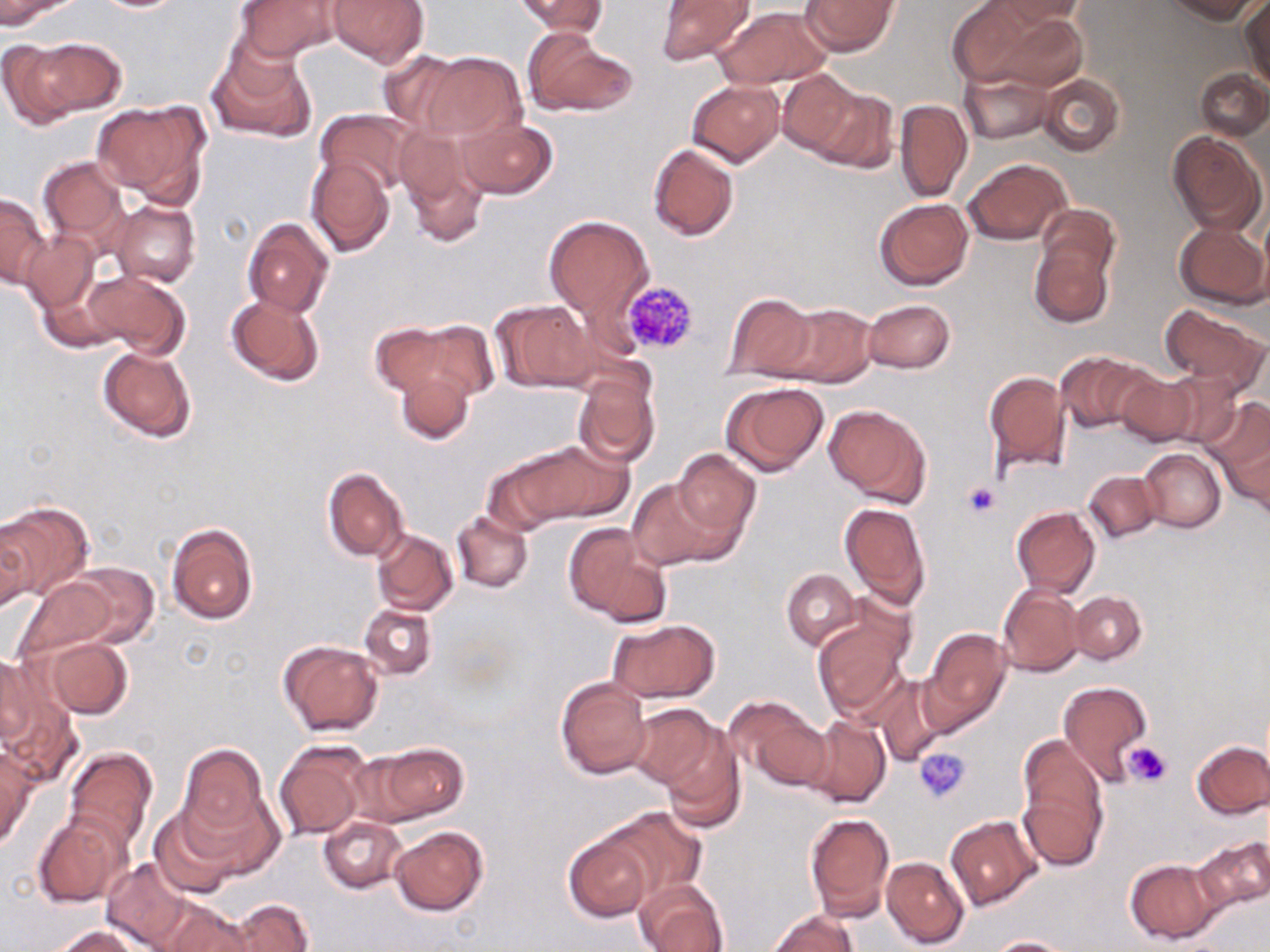
Approximate bounding boxes as named x1/y1/x2/y2 corners in pixels. Uninfected red blood cell locations: (x1=0, y1=0, x2=77, y2=30), (x1=88, y1=0, x2=191, y2=12), (x1=326, y1=0, x2=429, y2=68), (x1=515, y1=0, x2=608, y2=36), (x1=655, y1=0, x2=754, y2=66), (x1=801, y1=0, x2=899, y2=56), (x1=947, y1=0, x2=1043, y2=88), (x1=996, y1=0, x2=1089, y2=26), (x1=1161, y1=0, x2=1263, y2=23), (x1=236, y1=1, x2=342, y2=61), (x1=1240, y1=1, x2=1269, y2=85), (x1=715, y1=6, x2=829, y2=89), (x1=986, y1=10, x2=1090, y2=92), (x1=524, y1=29, x2=637, y2=118), (x1=16, y1=36, x2=124, y2=121), (x1=207, y1=42, x2=315, y2=144), (x1=377, y1=49, x2=468, y2=133), (x1=418, y1=52, x2=526, y2=142), (x1=959, y1=67, x2=1054, y2=144), (x1=1196, y1=69, x2=1269, y2=140), (x1=776, y1=70, x2=862, y2=156), (x1=1038, y1=74, x2=1124, y2=156), (x1=687, y1=79, x2=785, y2=166), (x1=801, y1=82, x2=895, y2=170), (x1=894, y1=99, x2=972, y2=204), (x1=92, y1=101, x2=211, y2=204), (x1=315, y1=109, x2=416, y2=198), (x1=457, y1=116, x2=560, y2=197), (x1=397, y1=125, x2=493, y2=245), (x1=1168, y1=132, x2=1265, y2=235), (x1=647, y1=143, x2=741, y2=241), (x1=36, y1=156, x2=130, y2=251), (x1=307, y1=156, x2=395, y2=257), (x1=963, y1=157, x2=1071, y2=245), (x1=1, y1=193, x2=49, y2=288), (x1=873, y1=198, x2=974, y2=290), (x1=112, y1=200, x2=200, y2=288), (x1=543, y1=215, x2=653, y2=323), (x1=242, y1=217, x2=334, y2=317), (x1=1174, y1=222, x2=1268, y2=310), (x1=23, y1=232, x2=99, y2=312), (x1=1028, y1=232, x2=1117, y2=330), (x1=84, y1=270, x2=189, y2=357), (x1=721, y1=292, x2=819, y2=380), (x1=226, y1=293, x2=325, y2=387), (x1=863, y1=298, x2=954, y2=374), (x1=493, y1=301, x2=600, y2=393), (x1=1159, y1=302, x2=1268, y2=390), (x1=772, y1=304, x2=877, y2=387), (x1=413, y1=319, x2=499, y2=403), (x1=370, y1=324, x2=458, y2=399), (x1=97, y1=345, x2=197, y2=442), (x1=1055, y1=351, x2=1154, y2=434), (x1=391, y1=364, x2=475, y2=446), (x1=983, y1=369, x2=1071, y2=474), (x1=1113, y1=369, x2=1199, y2=447), (x1=572, y1=370, x2=659, y2=468), (x1=1157, y1=372, x2=1245, y2=450), (x1=722, y1=381, x2=829, y2=476), (x1=1203, y1=396, x2=1269, y2=496), (x1=825, y1=404, x2=932, y2=508), (x1=1224, y1=428, x2=1270, y2=516), (x1=499, y1=441, x2=627, y2=527), (x1=1138, y1=447, x2=1225, y2=532), (x1=672, y1=448, x2=759, y2=542), (x1=322, y1=467, x2=409, y2=562), (x1=1084, y1=469, x2=1161, y2=543), (x1=628, y1=477, x2=722, y2=571), (x1=0, y1=500, x2=93, y2=599), (x1=839, y1=502, x2=932, y2=610), (x1=1011, y1=506, x2=1099, y2=597), (x1=452, y1=510, x2=534, y2=593), (x1=166, y1=523, x2=259, y2=627), (x1=0, y1=525, x2=34, y2=612), (x1=564, y1=525, x2=667, y2=626), (x1=373, y1=530, x2=458, y2=615), (x1=61, y1=563, x2=159, y2=650), (x1=782, y1=569, x2=861, y2=651), (x1=18, y1=578, x2=119, y2=659), (x1=996, y1=585, x2=1085, y2=677), (x1=1069, y1=591, x2=1147, y2=663), (x1=360, y1=603, x2=436, y2=679), (x1=813, y1=612, x2=912, y2=721), (x1=606, y1=619, x2=719, y2=703), (x1=921, y1=629, x2=1011, y2=732), (x1=45, y1=638, x2=131, y2=719), (x1=278, y1=640, x2=383, y2=736), (x1=0, y1=656, x2=33, y2=750), (x1=873, y1=675, x2=949, y2=767), (x1=555, y1=676, x2=652, y2=780), (x1=1058, y1=681, x2=1152, y2=782), (x1=2, y1=682, x2=81, y2=788), (x1=728, y1=698, x2=830, y2=790), (x1=627, y1=703, x2=723, y2=792), (x1=804, y1=716, x2=891, y2=808), (x1=659, y1=724, x2=746, y2=831), (x1=1017, y1=732, x2=1109, y2=869), (x1=275, y1=741, x2=370, y2=840), (x1=361, y1=741, x2=469, y2=825), (x1=1191, y1=741, x2=1270, y2=818), (x1=178, y1=744, x2=268, y2=839), (x1=64, y1=746, x2=157, y2=852), (x1=0, y1=747, x2=35, y2=850), (x1=181, y1=786, x2=283, y2=878), (x1=149, y1=807, x2=243, y2=899), (x1=593, y1=807, x2=704, y2=903), (x1=804, y1=811, x2=895, y2=919), (x1=33, y1=812, x2=131, y2=907), (x1=945, y1=814, x2=1041, y2=911), (x1=319, y1=817, x2=406, y2=893), (x1=390, y1=825, x2=489, y2=915), (x1=564, y1=827, x2=658, y2=921), (x1=1193, y1=834, x2=1270, y2=918), (x1=882, y1=856, x2=969, y2=947), (x1=101, y1=857, x2=195, y2=951), (x1=1125, y1=858, x2=1220, y2=944), (x1=633, y1=878, x2=729, y2=952), (x1=228, y1=899, x2=312, y2=952), (x1=156, y1=900, x2=252, y2=952), (x1=769, y1=910, x2=856, y2=952), (x1=53, y1=927, x2=142, y2=952), (x1=988, y1=936, x2=1072, y2=952). Platelet locations: (x1=622, y1=279, x2=700, y2=355), (x1=962, y1=481, x2=1002, y2=520), (x1=1124, y1=741, x2=1172, y2=786), (x1=915, y1=747, x2=972, y2=802). Slide-level diagnosis: no evidence of blood parasites. Thin blood film. Image is 1270×952 pixels. Light microscopy. May-Grünwald-Giemsa-stained preparation. Captured at 1000x magnification. One field of a larger specimen.